Assess the morphology of the red blood cells.
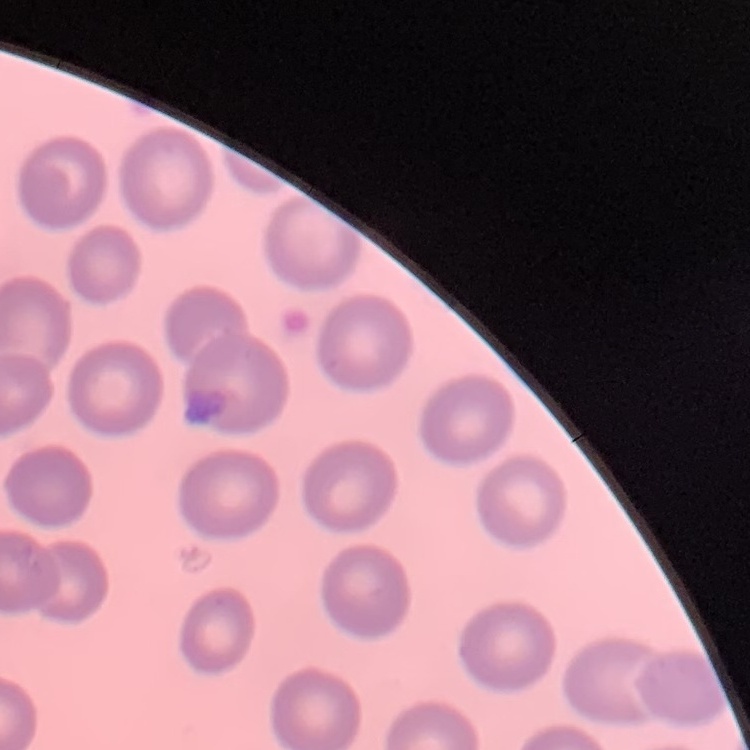
No rouleaux formation.

Summary:
  - Stain: Field's or Giemsa
  - Preparation: thin blood film
  - Image type: one tile cut from a larger photomicrograph